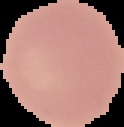

image_size: 124×127 pixels
image_type: cell region segmented out of the field of view; surrounding area masked to black
preparation: thin blood film
malaria_status: uninfected